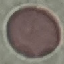

{
  "malaria_status": "uninfected",
  "image_type": "automatically extracted cell patch, resized to 64 × 64 pixels",
  "preparation": "thin smear",
  "stain": "Giemsa",
  "capture": "smartphone camera at the microscope eyepiece"
}